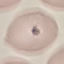

malaria status = parasitized
stain = Giemsa
image type = cell patch, automatically extracted from a larger field of view and resized to 64 × 64 pixels
preparation = thin blood film
capture = smartphone camera at the microscope eyepiece